State which parasite is depicted.
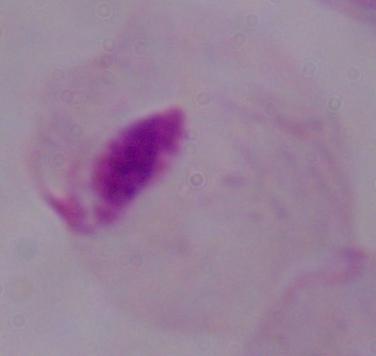
A trichomonad.

Photomicrograph. 1000x magnification.